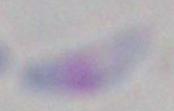

Summary:
  - Identification: Toxoplasma gondii
  - Magnification: 1000x
  - Modality: micrograph